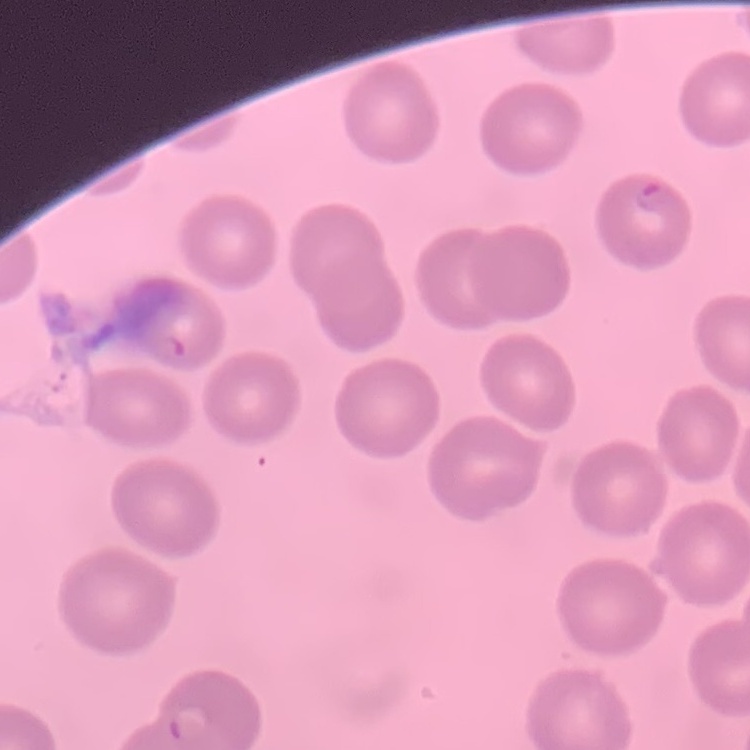

Summary:
  - Red blood cell morphology: no rouleaux formation
  - Image type: square crop of a larger photomicrograph
  - Stain: Field's or Giemsa
  - Preparation: thin blood film